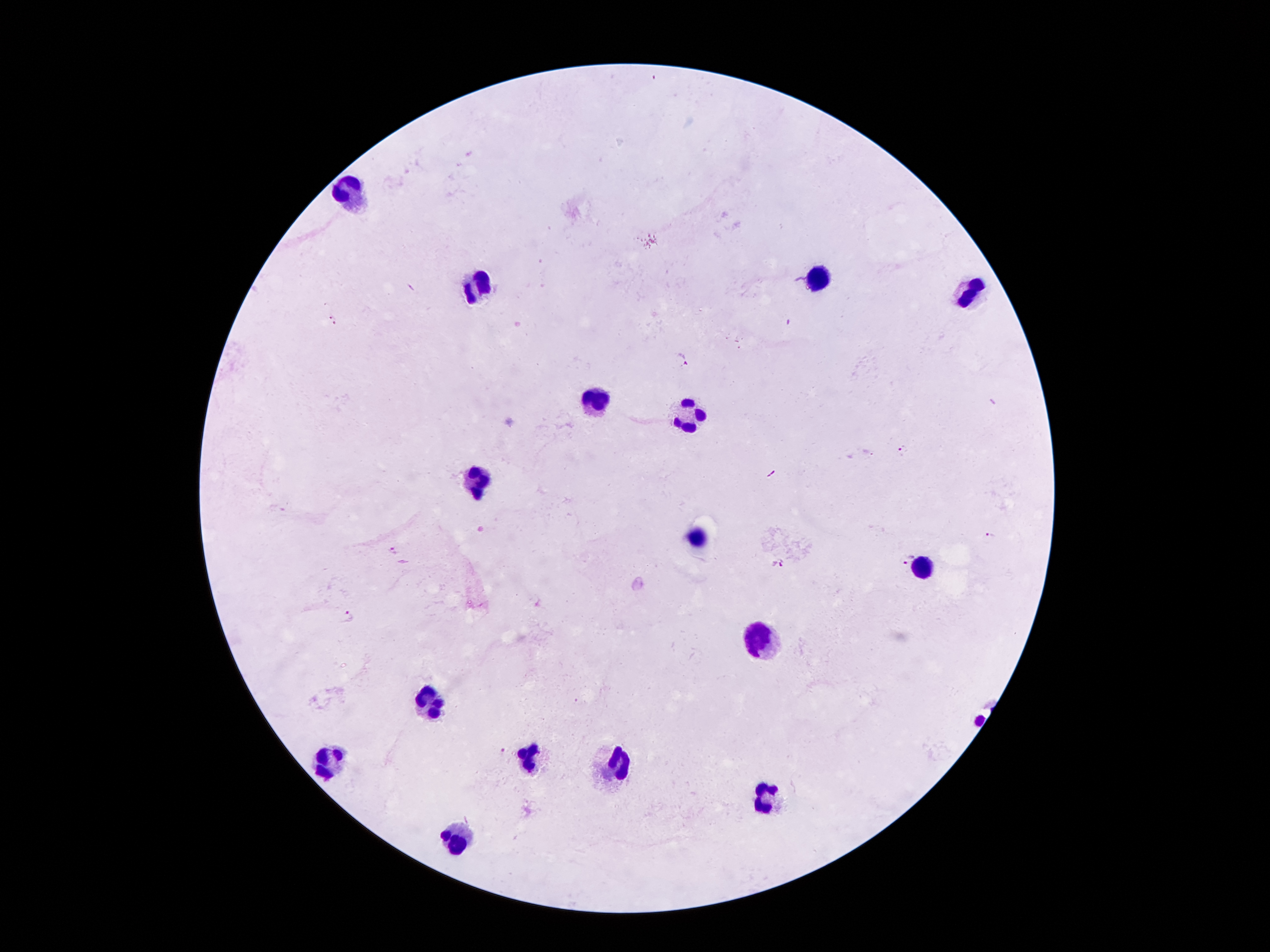

Approximate centers as (x, y) in pixels. Plasmodium parasite locations: (332, 319), (682, 357), (902, 451), (989, 536), (394, 550), (907, 558), (778, 565), (349, 615), (503, 751). Leukocyte locations: (352, 190), (816, 277), (477, 290), (966, 297), (597, 397), (692, 412), (480, 477), (699, 538), (925, 567), (763, 642), (430, 706), (529, 757), (328, 760), (617, 762), (770, 795), (460, 844). Patient malaria status: infected with Plasmodium falciparum. Image is 1270×952 pixels. Photographed through the microscope eyepiece with a smartphone camera. 100x magnification. Thick blood smear. Giemsa-stained preparation. Single field of view.